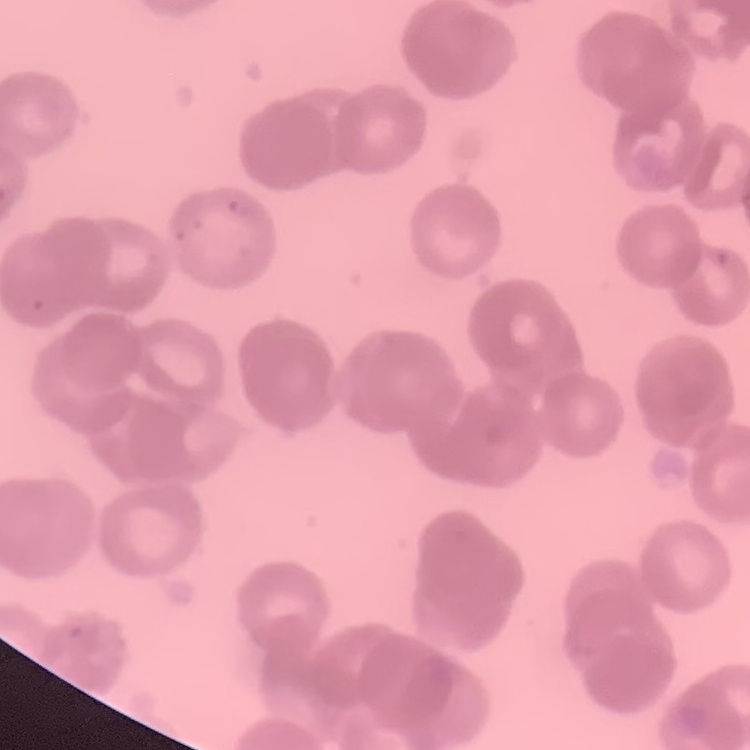

The erythrocytes exhibit rouleaux formation. Field's or Giemsa stain. Square crop of a larger photomicrograph. Thin blood film.